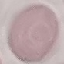

Summary:
  - Result: no malaria parasites seen
  - Image type: automatically extracted cell patch, resized to 64 × 64 pixels
  - Stain: Giemsa
  - Preparation: thin blood smear
  - Capture: smartphone camera at the microscope eyepiece